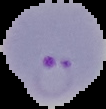 From a thin blood film. Result: Plasmodium parasites identified. Image is 106×109 pixels. Segmented cell region on a black background.